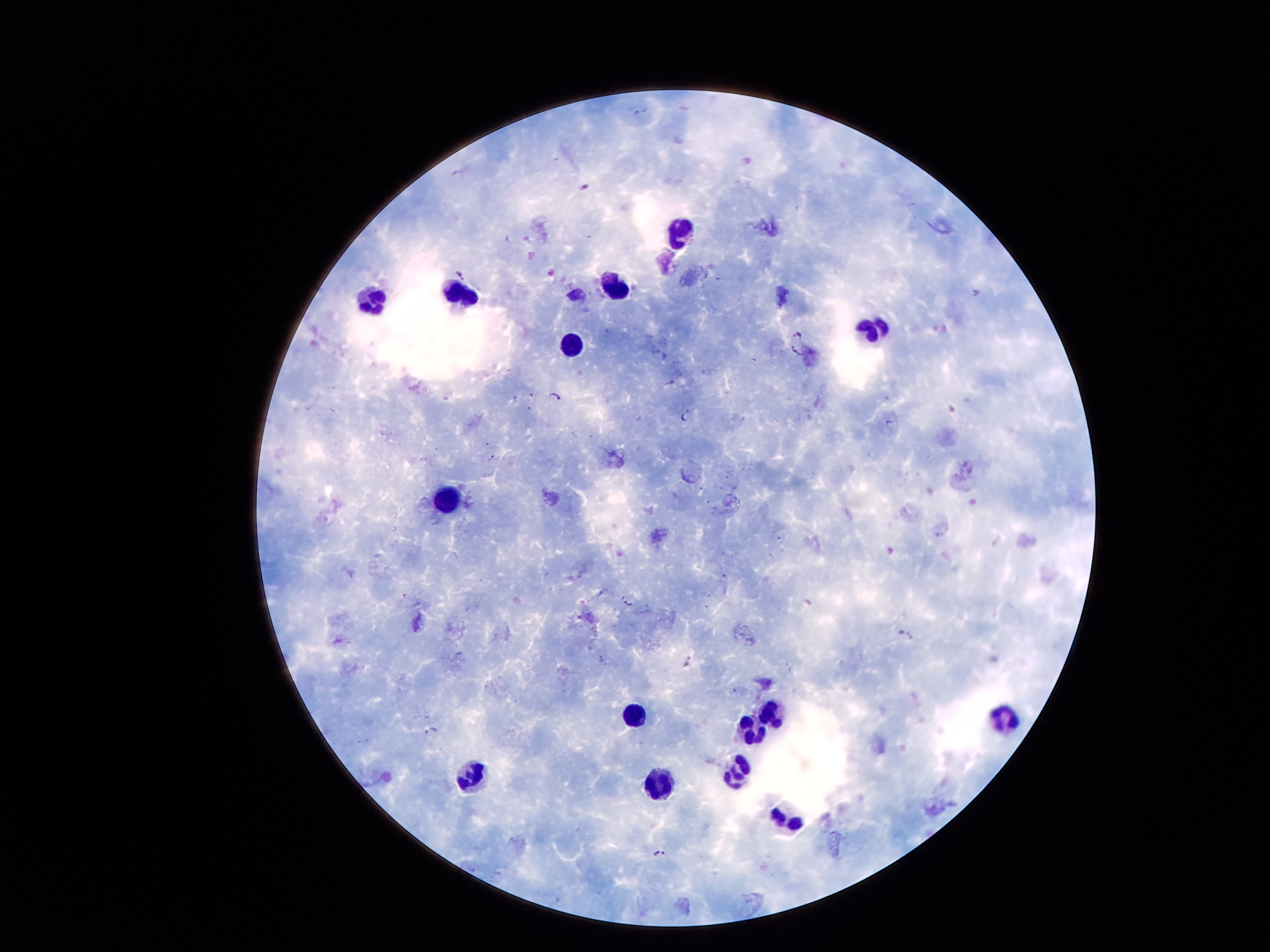 Approximate centers as [x, y] in pixels. Leukocyte locations: [679, 230], [617, 284], [457, 295], [373, 301], [869, 331], [571, 342], [444, 501], [771, 716], [630, 719], [1001, 719], [754, 735], [738, 771], [470, 777], [657, 785], [790, 824]. Plasmodium parasite locations: [460, 273], [796, 335], [797, 352], [660, 356], [555, 398], [685, 416], [492, 457], [626, 600], [908, 636], [432, 730], [659, 853]. Smartphone photograph taken through the microscope eyepiece. One field from this slide. 100x magnification. Giemsa-stained preparation. Patient malaria status: infected with Plasmodium falciparum. Thick blood smear. Image is 1270×952 pixels.